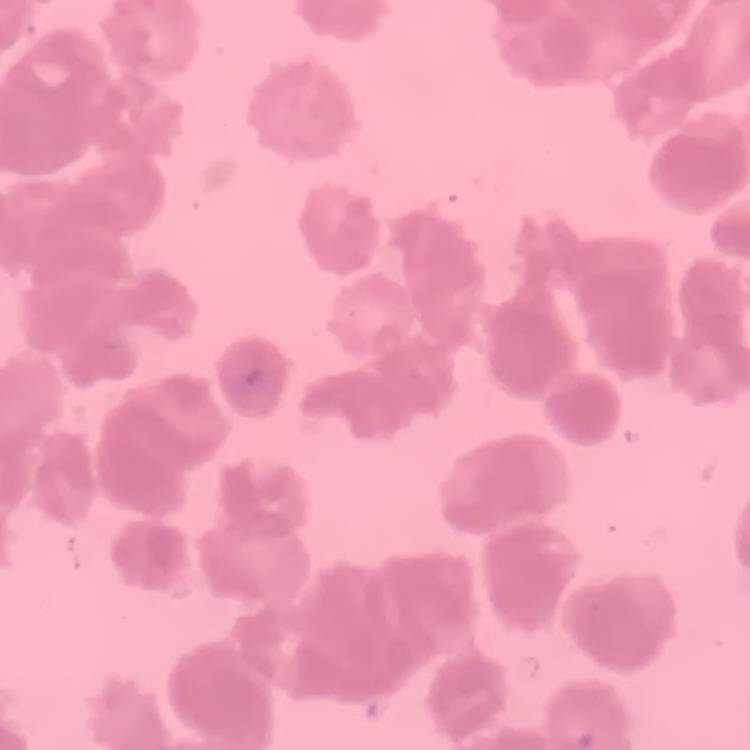

The red blood cells show rouleaux formation. Field's or Giemsa stain. Square crop of a larger photomicrograph. Thin blood smear.